State which parasite is depicted.
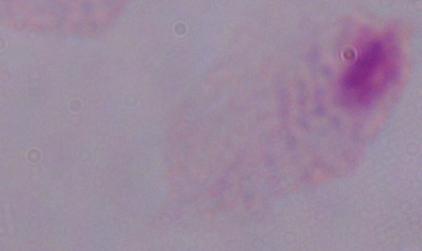
This is a trichomonad.

Captured at 1000x magnification. Micrograph.